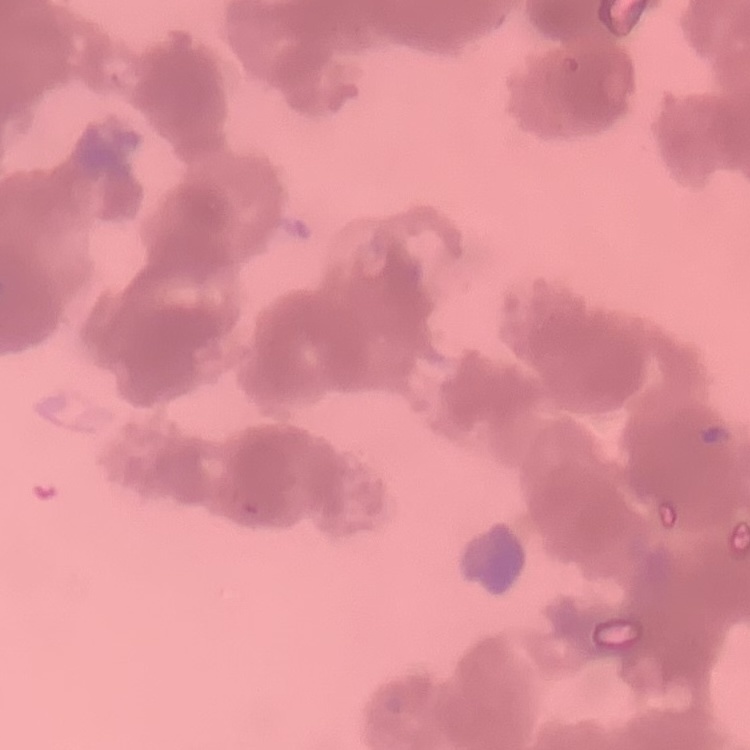
erythrocyte morphology = rouleaux formation
preparation = thin peripheral smear
image type = one tile cut from a larger photomicrograph
stain = Field's or Giemsa